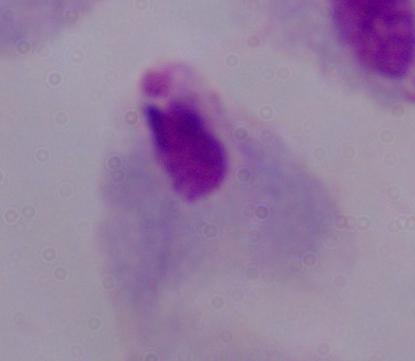

Photomicrograph. A trichomonad is shown. Captured at 1000x magnification.